Assess this cell for malaria.
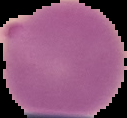
Parasitized.

preparation = thin blood film
image type = cell region segmented out of the field of view; surrounding area masked to black
image size = 127×118 pixels